Locate and identify every blood parasite.
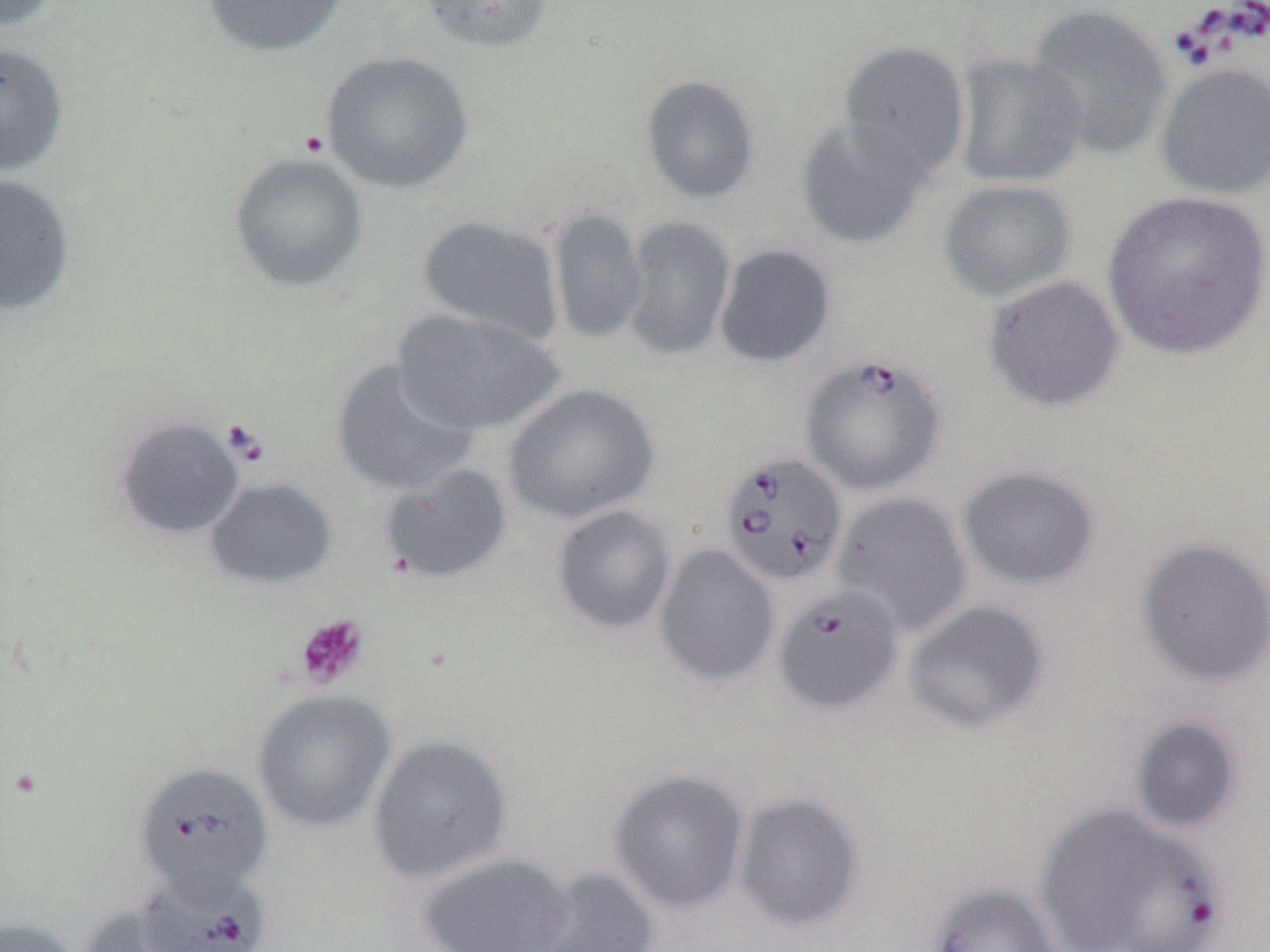

Approximate bounding boxes as (x1, y1, x2, y2) in pixels.
Babesia divergens-infected red blood cells: (800, 354, 947, 497), (717, 450, 848, 587), (774, 585, 904, 717), (133, 761, 273, 901), (1037, 804, 1218, 952), (136, 866, 272, 952).
No Plasmodium falciparum, Plasmodium ovale, Plasmodium malariae, Plasmodium vivax, or Trypanosoma brucei observed.

Summary:
  - Platelet locations: (295, 613, 370, 689)
  - Uninfected red blood cell locations: (200, 0, 349, 58), (417, 0, 554, 54), (1025, 4, 1172, 161), (0, 40, 71, 177), (838, 40, 970, 182), (320, 49, 474, 195), (952, 52, 1088, 189), (1155, 62, 1270, 200), (640, 74, 761, 205), (795, 116, 930, 251), (227, 150, 370, 295), (0, 172, 77, 317), (938, 179, 1077, 303), (1101, 190, 1270, 361), (547, 208, 647, 345), (416, 214, 564, 346), (623, 215, 736, 362), (714, 243, 837, 369), (984, 275, 1125, 412), (393, 307, 566, 437), (331, 357, 479, 497), (503, 383, 659, 524), (112, 415, 245, 541), (378, 463, 512, 585), (957, 465, 1100, 591), (204, 477, 337, 590), (832, 491, 973, 638), (552, 505, 676, 635), (1137, 537, 1270, 686), (655, 544, 779, 686), (904, 600, 1050, 735), (253, 689, 396, 832), (1128, 716, 1245, 834), (368, 734, 512, 883), (609, 769, 750, 914), (734, 793, 864, 934), (417, 852, 576, 952), (520, 868, 660, 952), (927, 883, 1067, 952), (76, 904, 194, 952), (0, 916, 80, 952)
  - Slide-level diagnosis: Babesia divergens
  - Preparation: thin blood film
  - Modality: light microscopy
  - Image size: 1270×952 pixels
  - Magnification: 1000x
  - Field of view: single
  - Stain: May-Grünwald-Giemsa